Report the malaria status of this cell.
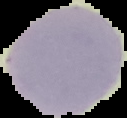
Uninfected.

image size = 127×118 pixels
preparation = thin blood smear
image type = segmented cell region with the area outside set to black